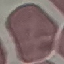

result: no malaria parasites seen
preparation: thin blood film
image_type: automatically extracted cell patch, resized to 64 × 64 pixels
capture: smartphone through the microscope eyepiece
stain: Giemsa